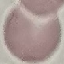
result = no malaria parasites detected
preparation = thin blood smear
image type = automatically extracted cell patch, resized to 64 × 64 pixels
stain = Giemsa
capture = smartphone camera at the microscope eyepiece